Report the malaria status of this cell.
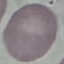

Uninfected.

preparation = thin blood film
capture = smartphone camera at the microscope eyepiece
stain = Giemsa
image type = automatically extracted cell patch, resized to 64 × 64 pixels